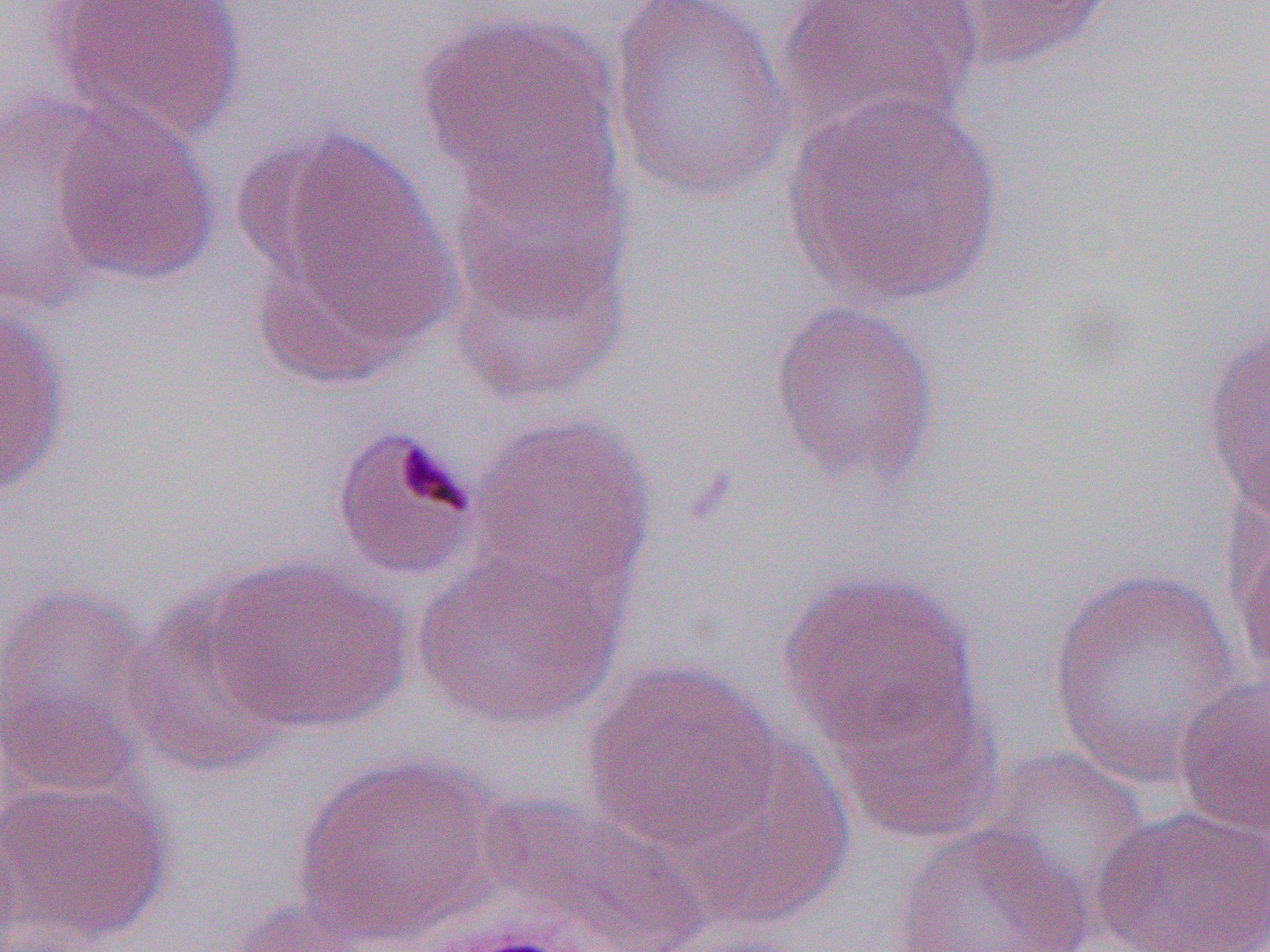

Approximate bounding boxes as [x1, y1, x2, y2] in pixels. Uninfected red blood cell locations: [45, 0, 249, 145], [773, 0, 984, 145], [923, 0, 1120, 74], [605, 2, 798, 204], [414, 8, 623, 211], [783, 89, 1005, 309], [0, 91, 119, 314], [48, 100, 219, 287], [244, 125, 460, 380], [441, 139, 635, 407], [769, 297, 942, 491], [0, 301, 71, 498], [1197, 314, 1270, 526], [465, 411, 656, 603], [330, 423, 481, 582], [1225, 488, 1270, 700], [414, 548, 625, 731], [204, 555, 411, 735], [1045, 566, 1249, 792], [776, 568, 981, 754], [0, 579, 162, 797], [122, 588, 300, 779], [579, 660, 782, 851], [822, 668, 1006, 847], [1172, 670, 1270, 842], [663, 736, 855, 932], [966, 746, 1153, 921], [287, 753, 504, 947], [0, 773, 175, 950], [465, 792, 713, 952], [1091, 804, 1270, 952], [0, 818, 22, 952], [886, 819, 1097, 952], [220, 895, 380, 952]. Slide-level diagnosis: Plasmodium malariae. Thin blood film. One field of a larger specimen. Captured at 1000x magnification. Image is 1270×952 pixels. Optical microscopy.